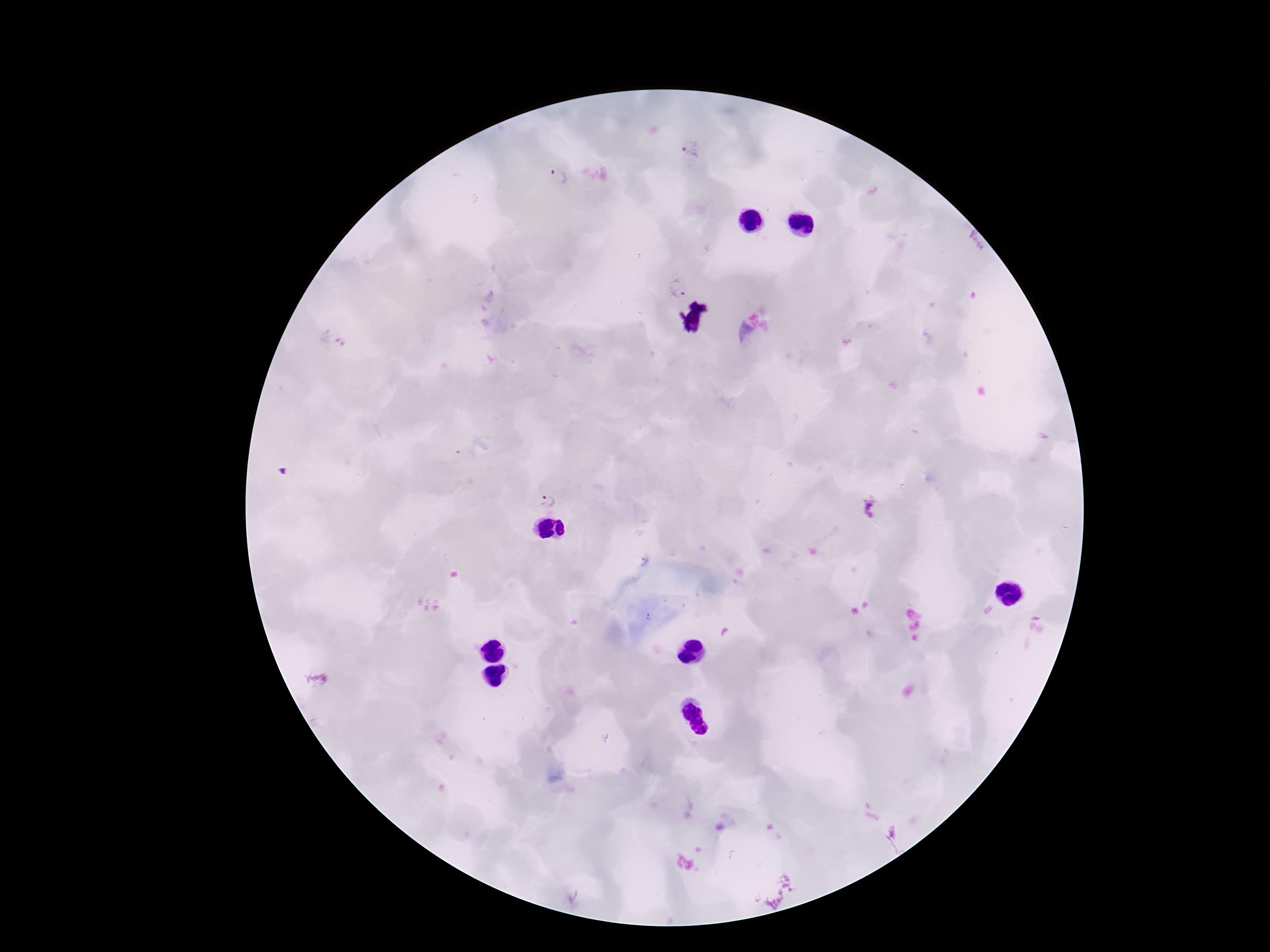

Approximate centers as (x, y) in pixels. Plasmodium parasite locations: (690, 148), (558, 178), (678, 288), (549, 501), (872, 507). Image is 1270×952 pixels. One field from this slide. Giemsa-stained preparation. Thick peripheral-blood smear. Patient malaria status: positive. Photographed through the microscope eyepiece with a smartphone camera. 100x magnification.